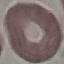

Summary:
  - Result: no malaria parasites detected
  - Preparation: thin smear
  - Image type: automatically extracted cell patch, resized to 64 × 64 pixels
  - Stain: Giemsa
  - Capture: smartphone camera at the microscope eyepiece